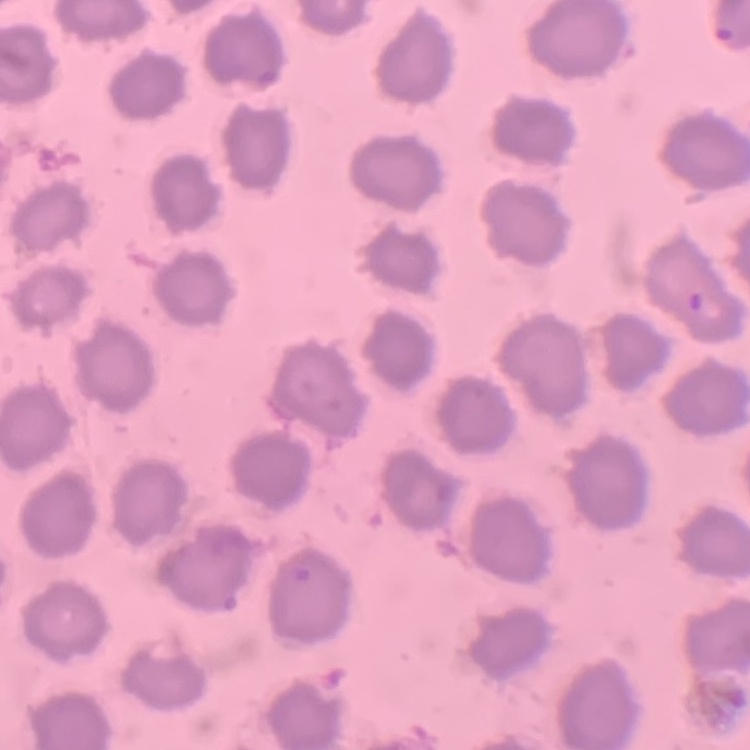

Summary:
  - Red blood cell morphology: no rouleaux formation
  - Stain: Field's or Giemsa
  - Image type: square crop of a larger photomicrograph
  - Preparation: thin peripheral smear